Locate and identify every blood parasite.
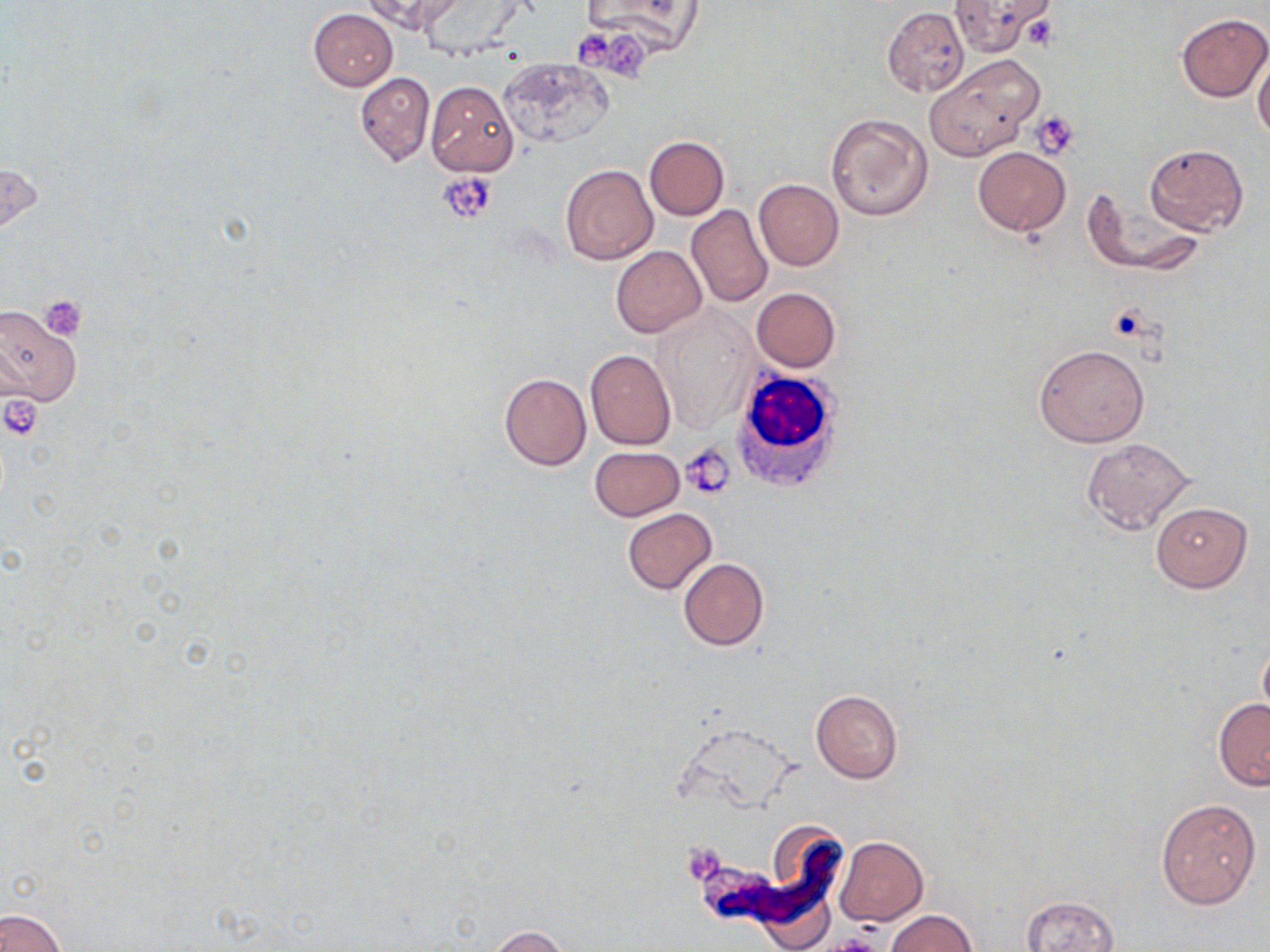

No blood parasites seen.

Approximate bounding boxes as (x1,y1)-(x2,y2) corner pairs in pixels. Uninfected red blood cell locations: (362,1)-(464,34), (579,1)-(707,54), (947,1)-(1054,57), (881,6)-(969,96), (308,8)-(398,90), (1176,13)-(1269,103), (1253,50)-(1270,143), (924,55)-(1043,161), (500,57)-(612,147), (354,71)-(434,166), (424,81)-(518,177), (824,113)-(933,221), (644,136)-(729,221), (1143,143)-(1249,235), (973,147)-(1071,237), (1,160)-(45,245), (560,163)-(658,264), (754,179)-(843,272), (1082,187)-(1207,277), (687,204)-(772,307), (610,245)-(708,338), (752,287)-(841,372), (0,303)-(82,407), (653,309)-(757,433), (1034,343)-(1150,447), (585,349)-(677,450), (499,372)-(591,471), (1080,437)-(1195,537), (589,446)-(685,521), (1151,501)-(1253,592), (622,508)-(716,595), (679,558)-(769,650), (1258,641)-(1270,722), (811,689)-(903,783), (1213,699)-(1270,790), (1155,798)-(1260,908), (834,836)-(929,925), (1021,894)-(1120,952), (0,908)-(66,952), (886,911)-(975,952), (483,925)-(571,951). White blood cell locations: (735,366)-(849,493). Platelet locations: (570,28)-(614,70), (608,32)-(653,81), (1032,112)-(1080,160), (440,173)-(498,222), (38,296)-(88,340), (681,444)-(736,500), (827,935)-(885,952). Slide-level diagnosis: negative for blood parasites. May-Grünwald-Giemsa-stained preparation. Image is 1270×952 pixels. Light microscopy. Single field of view. 1000x magnification. Thin blood smear.